Classify this cell by malaria status.
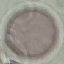
Uninfected.

Thin blood film. Automatically extracted cell patch, resized to 64 × 64 pixels. Acquired by smartphone through the microscope eyepiece. Giemsa-stained preparation.